Describe the morphology of the red blood cells.
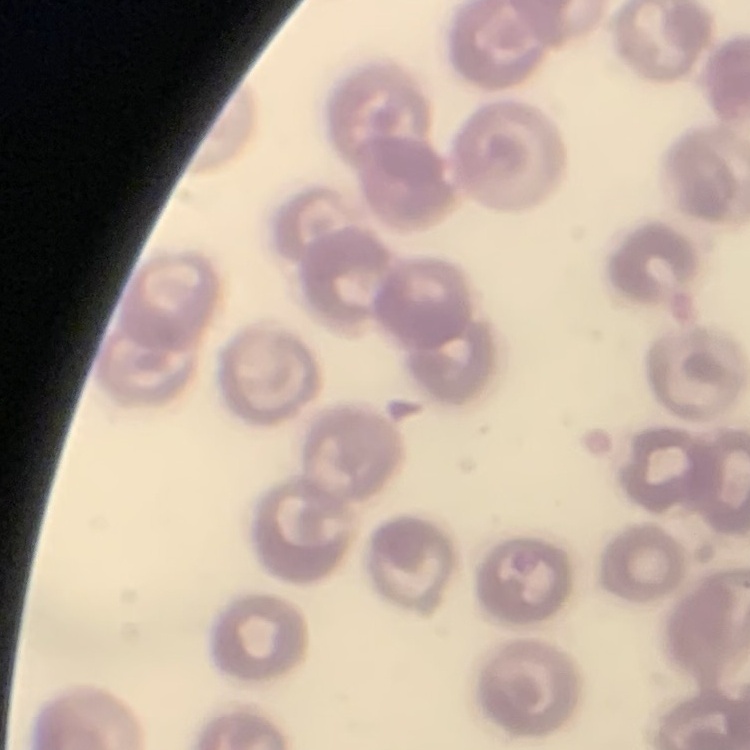

No rouleaux formation.

Stained with either Field's or Giemsa. Square crop of a larger photomicrograph. Thin blood film.